Assess this cell for malaria.
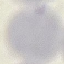
Uninfected.

Thin smear of blood. Automatically extracted cell patch, resized to 64 × 64 pixels. Giemsa-stained preparation. Acquired by smartphone through the microscope eyepiece.